Locate malaria parasites and leukocytes.
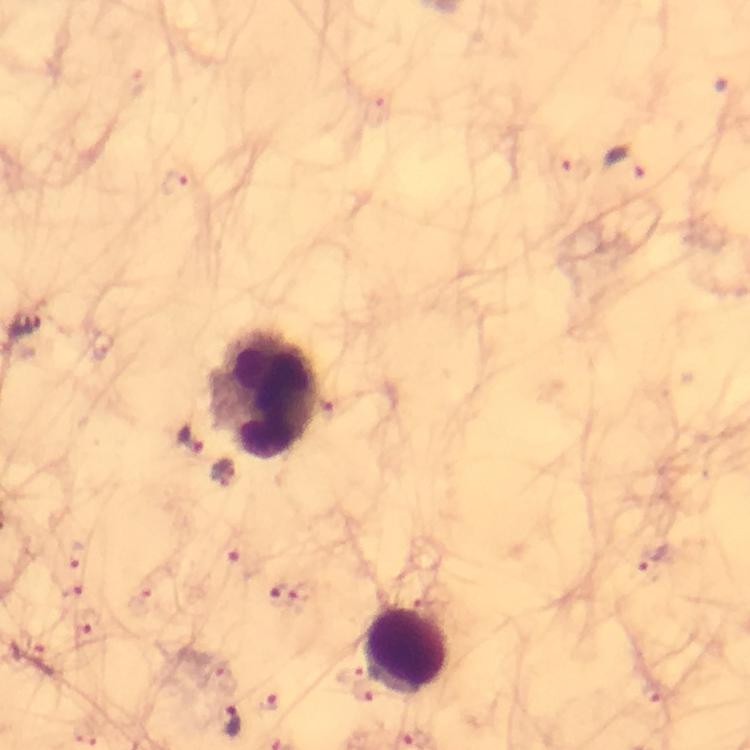
Approximate centers as {x, y} in pixels.
Malaria parasites: {624, 161}, {558, 163}, {174, 183}, {25, 326}, {188, 443}, {221, 473}, {77, 555}, {236, 560}, {656, 562}, {71, 591}, {282, 594}, {86, 622}, {37, 653}, {348, 671}, {654, 693}, {363, 695}, {268, 701}, {233, 720}.
Leukocytes: {260, 393}, {406, 652}.

{
  "magnification": "100x",
  "immersion_oil": "used",
  "stain": "Giemsa",
  "preparation": "thick blood film",
  "capture": "smartphone mounted on the microscope",
  "context": "from a malaria diagnostic workup",
  "cropped_from": "a single field of view",
  "image_size": "750×750 pixels"
}